Locate every blood parasite and identify its species.
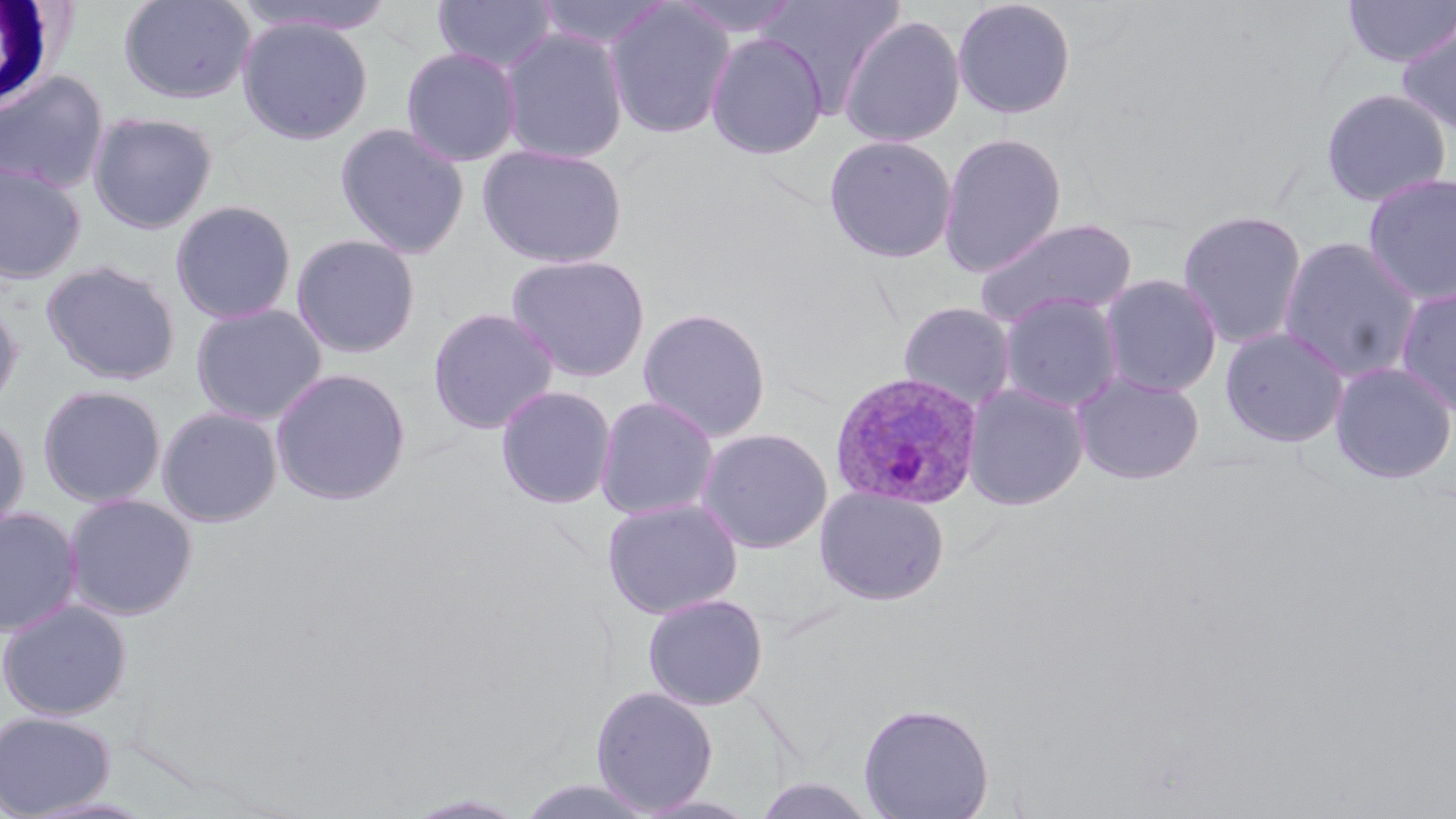

Approximate bounding boxes as named x1/y1/x2/y2 corners in pixels.
Plasmodium ovale-infected red blood cells: (x1=830, y1=370, x2=984, y2=511).
No Plasmodium falciparum, Plasmodium malariae, Plasmodium vivax, Babesia divergens, or Trypanosoma brucei observed.

White blood cell locations: (x1=0, y1=0, x2=69, y2=110). Uninfected red blood cell locations: (x1=118, y1=0, x2=256, y2=104), (x1=233, y1=0, x2=399, y2=38), (x1=432, y1=0, x2=559, y2=75), (x1=534, y1=0, x2=673, y2=54), (x1=671, y1=0, x2=805, y2=39), (x1=757, y1=0, x2=907, y2=117), (x1=951, y1=0, x2=1077, y2=120), (x1=1342, y1=0, x2=1456, y2=68), (x1=603, y1=1, x2=736, y2=140), (x1=122, y1=8, x2=375, y2=119), (x1=838, y1=14, x2=966, y2=148), (x1=237, y1=16, x2=374, y2=145), (x1=1395, y1=19, x2=1456, y2=137), (x1=499, y1=28, x2=631, y2=164), (x1=705, y1=32, x2=829, y2=160), (x1=400, y1=46, x2=523, y2=168), (x1=0, y1=69, x2=111, y2=193), (x1=1320, y1=88, x2=1452, y2=207), (x1=87, y1=111, x2=218, y2=234), (x1=334, y1=121, x2=471, y2=259), (x1=938, y1=131, x2=1068, y2=277), (x1=823, y1=134, x2=959, y2=264), (x1=476, y1=143, x2=628, y2=268), (x1=0, y1=160, x2=87, y2=284), (x1=1362, y1=172, x2=1456, y2=307), (x1=170, y1=199, x2=297, y2=324), (x1=1176, y1=208, x2=1309, y2=349), (x1=973, y1=217, x2=1140, y2=329), (x1=290, y1=233, x2=422, y2=359), (x1=1277, y1=236, x2=1423, y2=382), (x1=506, y1=253, x2=652, y2=382), (x1=40, y1=260, x2=181, y2=386), (x1=1099, y1=274, x2=1223, y2=396), (x1=1395, y1=284, x2=1456, y2=418), (x1=997, y1=292, x2=1124, y2=413), (x1=0, y1=298, x2=24, y2=417), (x1=897, y1=301, x2=1017, y2=411), (x1=190, y1=303, x2=328, y2=426), (x1=637, y1=306, x2=772, y2=442), (x1=427, y1=307, x2=559, y2=435), (x1=1220, y1=326, x2=1350, y2=448), (x1=1330, y1=361, x2=1456, y2=484), (x1=270, y1=367, x2=412, y2=506), (x1=1072, y1=371, x2=1205, y2=485), (x1=963, y1=381, x2=1089, y2=510), (x1=36, y1=384, x2=167, y2=508), (x1=495, y1=385, x2=617, y2=509), (x1=594, y1=395, x2=721, y2=521), (x1=156, y1=405, x2=284, y2=527), (x1=0, y1=414, x2=31, y2=538), (x1=696, y1=427, x2=833, y2=554), (x1=815, y1=486, x2=950, y2=606), (x1=63, y1=492, x2=198, y2=620), (x1=602, y1=498, x2=744, y2=619), (x1=0, y1=506, x2=84, y2=637), (x1=642, y1=592, x2=769, y2=710), (x1=0, y1=598, x2=132, y2=721), (x1=590, y1=685, x2=718, y2=814), (x1=857, y1=701, x2=995, y2=819), (x1=0, y1=710, x2=116, y2=817), (x1=750, y1=775, x2=882, y2=819), (x1=514, y1=777, x2=661, y2=819), (x1=405, y1=793, x2=530, y2=818), (x1=633, y1=794, x2=765, y2=818). Slide-level diagnosis: Plasmodium ovale. Single field of view. Thin blood film. May-Grünwald-Giemsa stain. 1000x magnification. Image is 1456×819 pixels. Light microscopy.